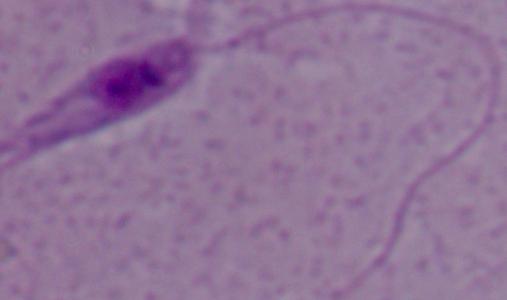
A Leishmania parasite is seen. Micrograph. 1000x magnification.